Comment on the morphology of the red blood cells.
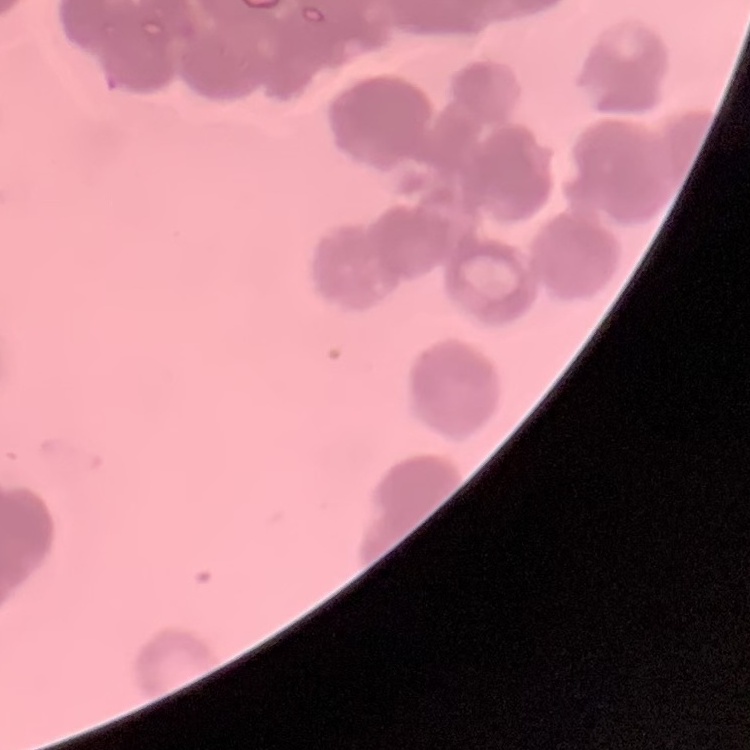
Rouleaux formation.

Thin blood smear. Square crop of a larger photomicrograph. Field's or Giemsa stain.